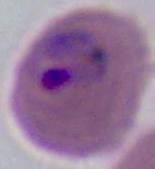
Summary:
  - Magnification: 400x or 1000x
  - Modality: micrograph
  - Identification: Plasmodium